Locate every cell, classifying each as a parasitized RBC, an uninfected RBC, or a WBC.
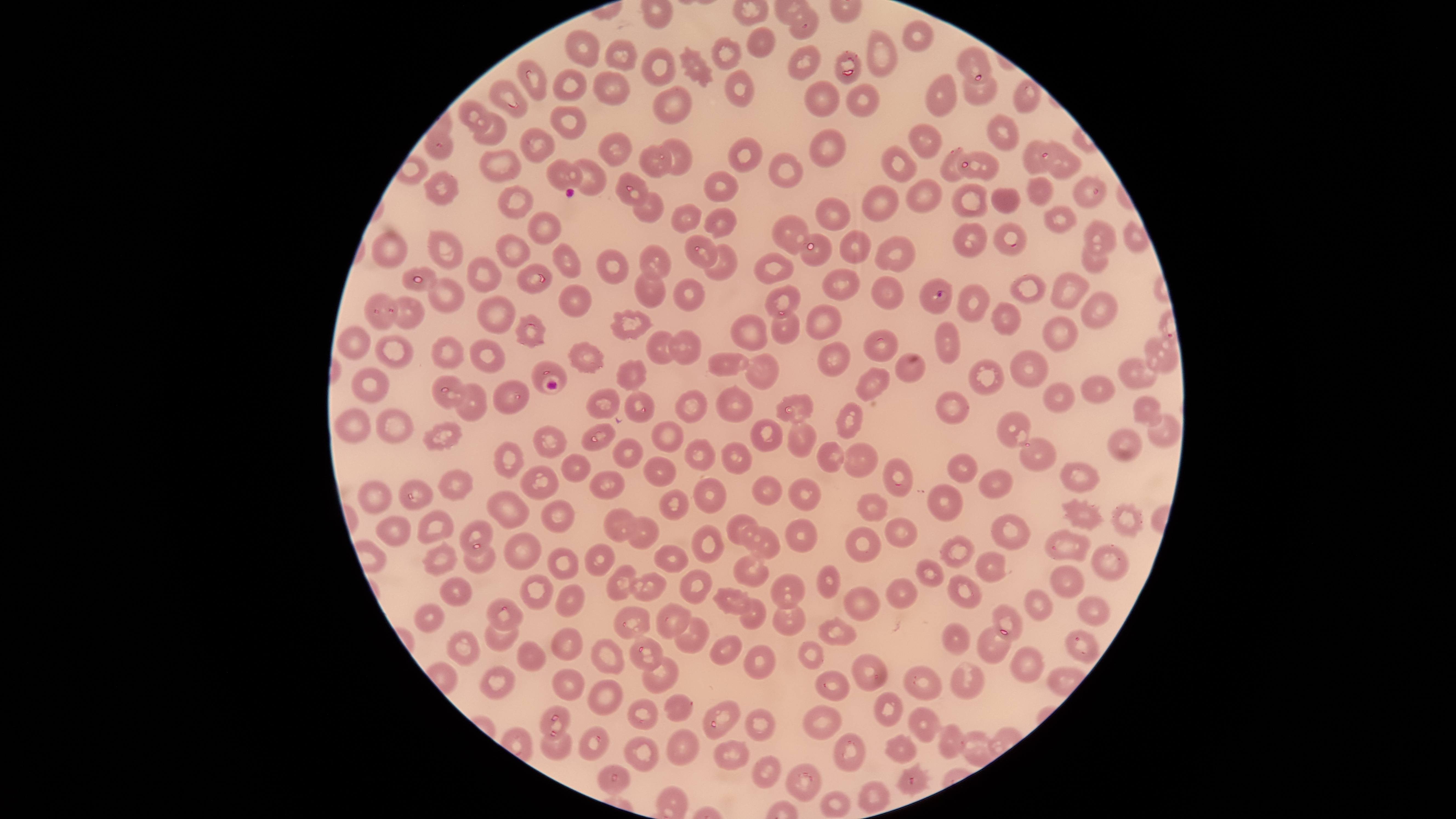
Approximate bounding boxes as [left, top, right, bottom] in pixels.
Parasitized RBCs: [919, 278, 953, 314].
Uninfected RBCs: [788, 4, 819, 41], [901, 20, 936, 52], [565, 26, 600, 69], [746, 26, 775, 58], [865, 28, 899, 79], [710, 36, 742, 70], [604, 38, 639, 71], [787, 44, 823, 82], [954, 44, 993, 85], [678, 46, 714, 87], [640, 47, 677, 88], [834, 49, 862, 85], [517, 59, 547, 102], [553, 69, 586, 102], [724, 69, 755, 109], [591, 72, 630, 105], [925, 72, 957, 117], [960, 73, 997, 106], [1013, 78, 1042, 114], [489, 80, 529, 118], [804, 80, 841, 118], [845, 82, 881, 117], [651, 85, 693, 124], [458, 100, 491, 133], [549, 105, 587, 140], [473, 112, 508, 147], [986, 113, 1020, 151], [908, 121, 942, 159], [519, 126, 556, 163], [808, 128, 848, 166], [424, 130, 455, 161], [597, 132, 633, 166], [727, 137, 764, 173], [659, 138, 693, 176], [1022, 138, 1061, 175], [1039, 142, 1082, 180], [638, 143, 673, 178], [881, 145, 919, 183], [940, 146, 969, 182], [477, 148, 523, 184], [955, 151, 999, 182], [769, 152, 803, 188], [546, 158, 584, 191], [568, 158, 607, 197], [423, 170, 459, 207], [704, 170, 739, 203], [613, 172, 649, 208], [1072, 175, 1108, 210], [1026, 176, 1054, 208], [904, 179, 944, 214], [951, 182, 989, 219], [860, 184, 900, 221], [497, 185, 533, 220], [991, 188, 1022, 214], [632, 191, 665, 222], [816, 198, 852, 231], [671, 203, 702, 233], [703, 206, 739, 239], [1043, 206, 1076, 233], [527, 211, 561, 245], [771, 214, 810, 256], [1083, 219, 1118, 257], [1122, 220, 1151, 253], [992, 221, 1029, 257], [951, 222, 989, 258], [427, 229, 464, 272], [838, 229, 873, 265], [370, 231, 409, 269], [496, 233, 531, 269], [799, 233, 833, 266], [683, 235, 718, 269], [874, 235, 916, 273], [1081, 242, 1109, 276], [550, 243, 581, 280], [637, 243, 671, 279], [703, 244, 739, 281], [596, 248, 630, 286], [753, 250, 794, 285], [466, 256, 503, 294], [516, 264, 554, 295], [400, 267, 438, 291], [822, 268, 861, 301], [634, 271, 667, 309], [1048, 271, 1091, 311], [1008, 272, 1047, 306], [870, 276, 906, 310], [427, 277, 468, 314], [673, 278, 706, 312], [557, 283, 592, 318], [957, 283, 990, 323], [764, 285, 802, 319], [1079, 290, 1118, 331], [364, 292, 398, 331], [389, 296, 425, 329], [476, 296, 518, 335], [990, 301, 1023, 336], [806, 303, 843, 340], [610, 309, 655, 340], [770, 310, 800, 345], [513, 312, 548, 349], [730, 313, 768, 352], [1041, 314, 1081, 353], [934, 321, 960, 365], [336, 324, 372, 361], [863, 328, 898, 363], [645, 330, 680, 365], [667, 330, 702, 366], [374, 333, 415, 369], [429, 336, 465, 370], [467, 337, 506, 375], [1144, 337, 1178, 375], [565, 340, 606, 374], [816, 341, 852, 377], [1009, 349, 1050, 388], [707, 351, 751, 378], [894, 351, 927, 383], [745, 353, 781, 390], [615, 358, 648, 392], [1118, 358, 1161, 389], [968, 359, 1005, 396], [351, 366, 389, 403], [855, 366, 891, 402], [431, 375, 465, 409], [1080, 376, 1117, 404], [492, 380, 529, 416], [453, 382, 488, 423], [1041, 382, 1076, 414], [715, 384, 755, 422], [585, 388, 621, 420], [674, 388, 707, 424], [624, 390, 656, 423], [935, 390, 970, 425], [775, 393, 814, 424], [1132, 395, 1163, 427], [833, 402, 865, 440], [333, 408, 371, 444], [375, 408, 415, 445], [995, 409, 1033, 449], [1149, 413, 1180, 450], [749, 418, 784, 454], [650, 419, 684, 453], [421, 420, 463, 452], [786, 421, 819, 460], [580, 423, 616, 451], [532, 424, 568, 459], [1106, 428, 1143, 463], [611, 436, 646, 469], [684, 438, 716, 471], [1019, 438, 1057, 472], [491, 440, 525, 481], [720, 441, 753, 474], [816, 441, 845, 473], [842, 442, 879, 480], [946, 451, 979, 483], [559, 452, 592, 483], [643, 454, 677, 488], [882, 458, 912, 499], [1059, 461, 1100, 493], [520, 464, 560, 501], [437, 468, 473, 502], [978, 469, 1014, 499], [589, 470, 625, 500], [752, 474, 785, 507], [692, 476, 727, 514], [788, 477, 822, 510], [357, 478, 393, 516], [398, 478, 433, 511], [926, 483, 964, 522], [486, 489, 530, 531], [658, 489, 690, 521], [854, 492, 888, 522], [1060, 497, 1106, 532], [539, 499, 575, 533], [1110, 501, 1145, 540], [603, 507, 637, 543], [416, 509, 455, 546], [726, 512, 760, 545], [991, 512, 1032, 551], [375, 515, 412, 548], [626, 516, 661, 549], [884, 516, 919, 550], [784, 517, 819, 552], [458, 519, 494, 558], [691, 524, 726, 564], [741, 524, 782, 560], [845, 526, 882, 563], [1045, 527, 1093, 563], [503, 532, 541, 571], [939, 534, 975, 570], [420, 541, 459, 578], [1092, 542, 1131, 582], [463, 543, 499, 575], [584, 543, 617, 577], [652, 544, 690, 575], [546, 547, 580, 580], [974, 551, 1013, 583], [732, 554, 771, 588], [916, 557, 945, 587], [817, 564, 841, 599], [1049, 564, 1086, 600], [604, 565, 637, 602], [680, 569, 713, 604], [628, 572, 667, 602], [519, 573, 555, 611], [769, 573, 806, 610], [946, 573, 984, 609], [439, 577, 473, 606], [885, 577, 919, 610], [554, 582, 585, 617], [712, 586, 752, 616], [843, 586, 882, 621], [1023, 588, 1054, 621], [1077, 596, 1110, 627], [485, 597, 524, 630], [738, 597, 767, 630], [413, 602, 445, 633], [655, 602, 693, 640], [773, 602, 808, 638], [989, 603, 1024, 641], [613, 605, 651, 641], [818, 615, 856, 646], [674, 617, 711, 654], [942, 621, 973, 656], [484, 623, 519, 653], [976, 624, 1012, 664], [550, 627, 584, 661], [1065, 628, 1100, 665], [445, 630, 481, 667], [629, 635, 664, 672], [709, 635, 743, 666], [590, 637, 626, 675], [516, 640, 549, 672], [797, 640, 824, 670], [742, 644, 776, 681], [1008, 644, 1045, 683], [849, 653, 888, 693], [642, 656, 680, 693], [950, 660, 985, 699], [902, 664, 943, 701], [478, 665, 516, 700], [552, 667, 586, 702], [815, 670, 850, 701], [587, 678, 624, 716], [874, 691, 904, 727], [662, 693, 693, 722], [626, 697, 659, 731], [703, 701, 740, 739], [539, 704, 571, 740], [802, 704, 844, 741], [744, 708, 775, 743], [908, 708, 941, 741], [937, 723, 968, 760], [577, 726, 611, 761], [666, 728, 699, 766], [539, 730, 574, 760], [960, 731, 996, 768], [833, 732, 867, 773], [883, 733, 916, 764], [622, 736, 658, 771], [713, 739, 749, 770], [752, 755, 782, 789], [895, 761, 933, 798], [596, 762, 631, 795], [786, 762, 821, 802], [858, 780, 892, 814], [819, 789, 852, 818].
No WBCs identified.

field of view = single
visible region = circular
preparation = thin blood film
stain = Giemsa
image size = 1456×819 pixels
species = Plasmodium falciparum
capture = smartphone photograph through the microscope eyepiece